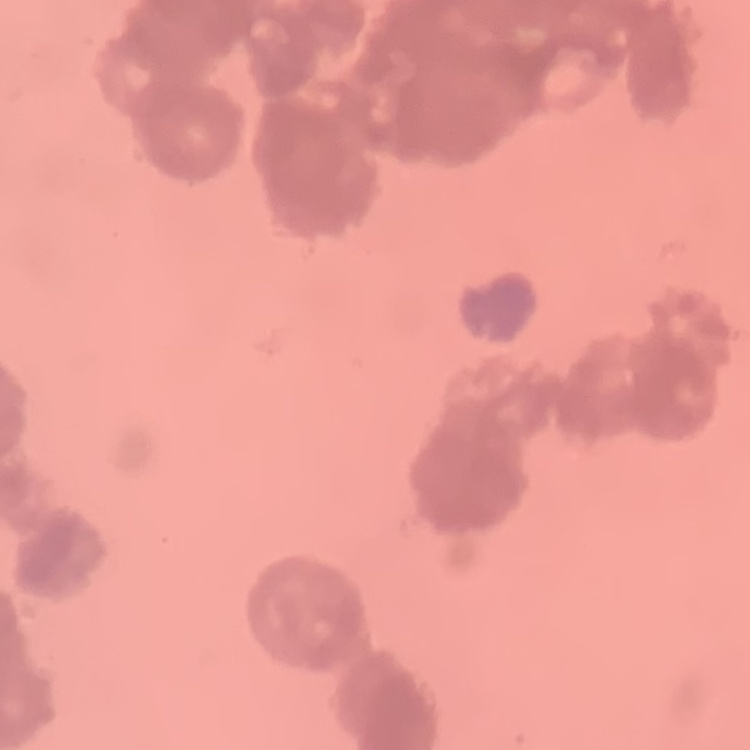

The erythrocytes show rouleaux formation. Field's or Giemsa stain. Square crop of a larger photomicrograph. Thin blood smear.